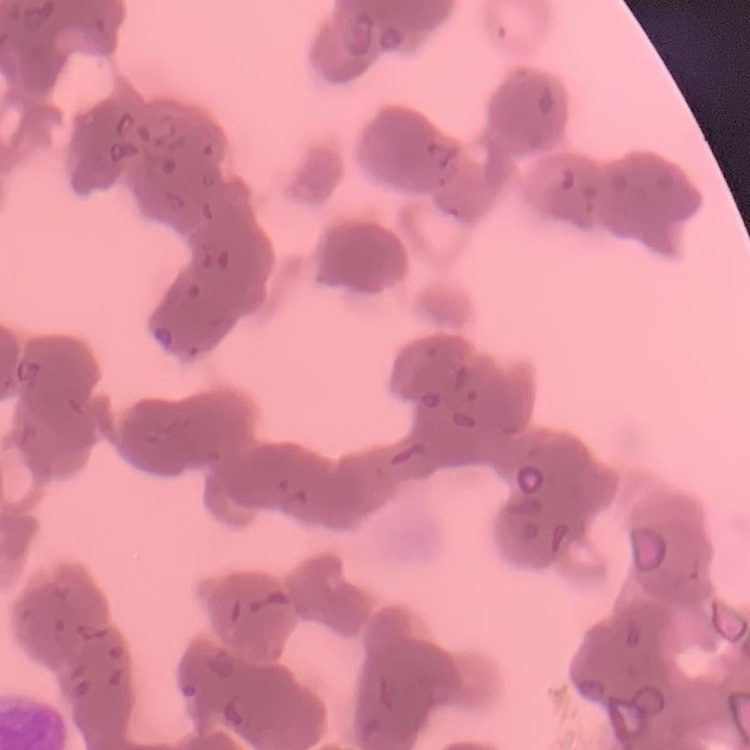
red blood cell morphology = rouleaux formation
stain = Field's or Giemsa
preparation = thin blood smear
image type = one tile cut from a larger photomicrograph